Locate every Plasmodium parasite.
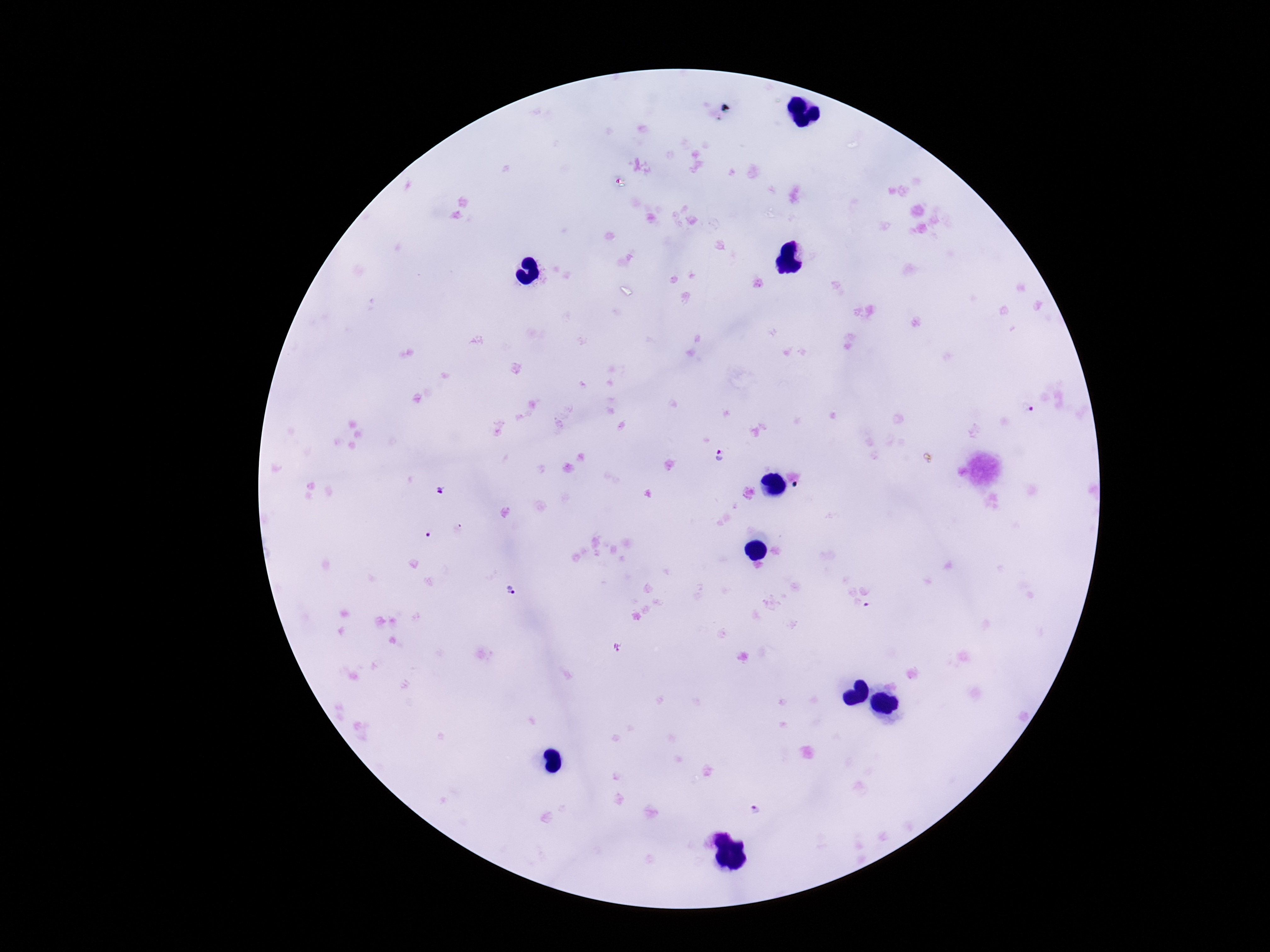
Approximate centers as [x, y] in pixels.
Plasmodium parasites: [1026, 407], [721, 457], [513, 591], [755, 811].

Summary:
  - Preparation: thick blood smear
  - Patient malaria status: positive
  - Stain: Giemsa
  - Field of view: one from this slide
  - Magnification: 100x
  - Capture: smartphone camera through the microscope eyepiece
  - Image size: 1270×952 pixels